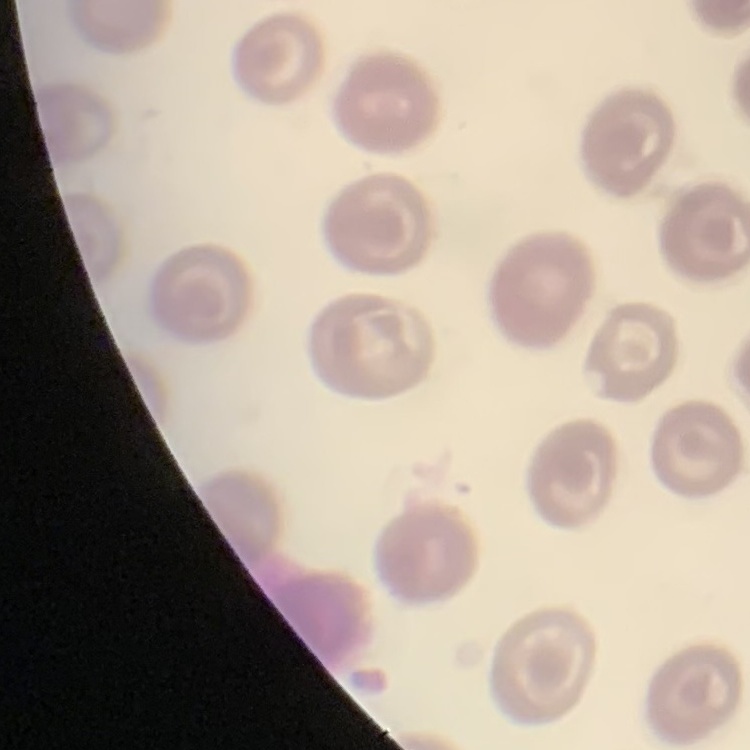

red blood cell morphology = no rouleaux formation
image type = one tile cut from a larger photomicrograph
stain = Field's or Giemsa
preparation = thin blood smear